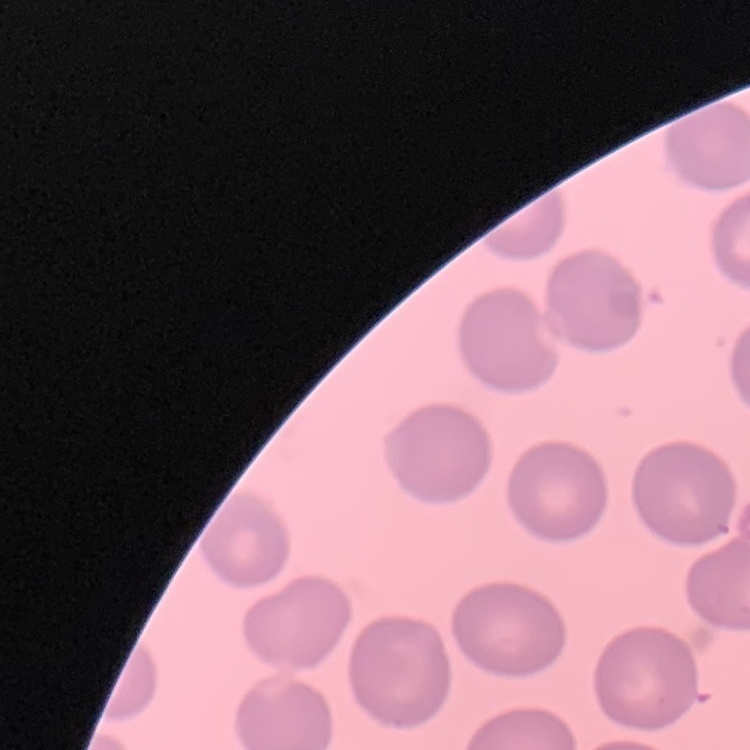
Summary:
  - Red blood cell morphology: no rouleaux formation
  - Preparation: thin peripheral smear
  - Image type: square crop of a larger photomicrograph
  - Stain: Field's or Giemsa